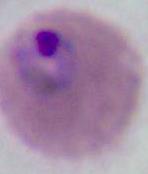

Summary:
  - Modality: micrograph
  - Identification: Plasmodium
  - Magnification: 400x or 1000x